Classify this cell by malaria status.
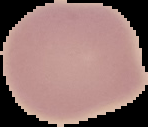

Uninfected.

preparation = thin blood film
image type = segmented cell region on a black background
image size = 148×127 pixels